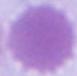

Photomicrograph. A red blood cell is shown. 1000x magnification.